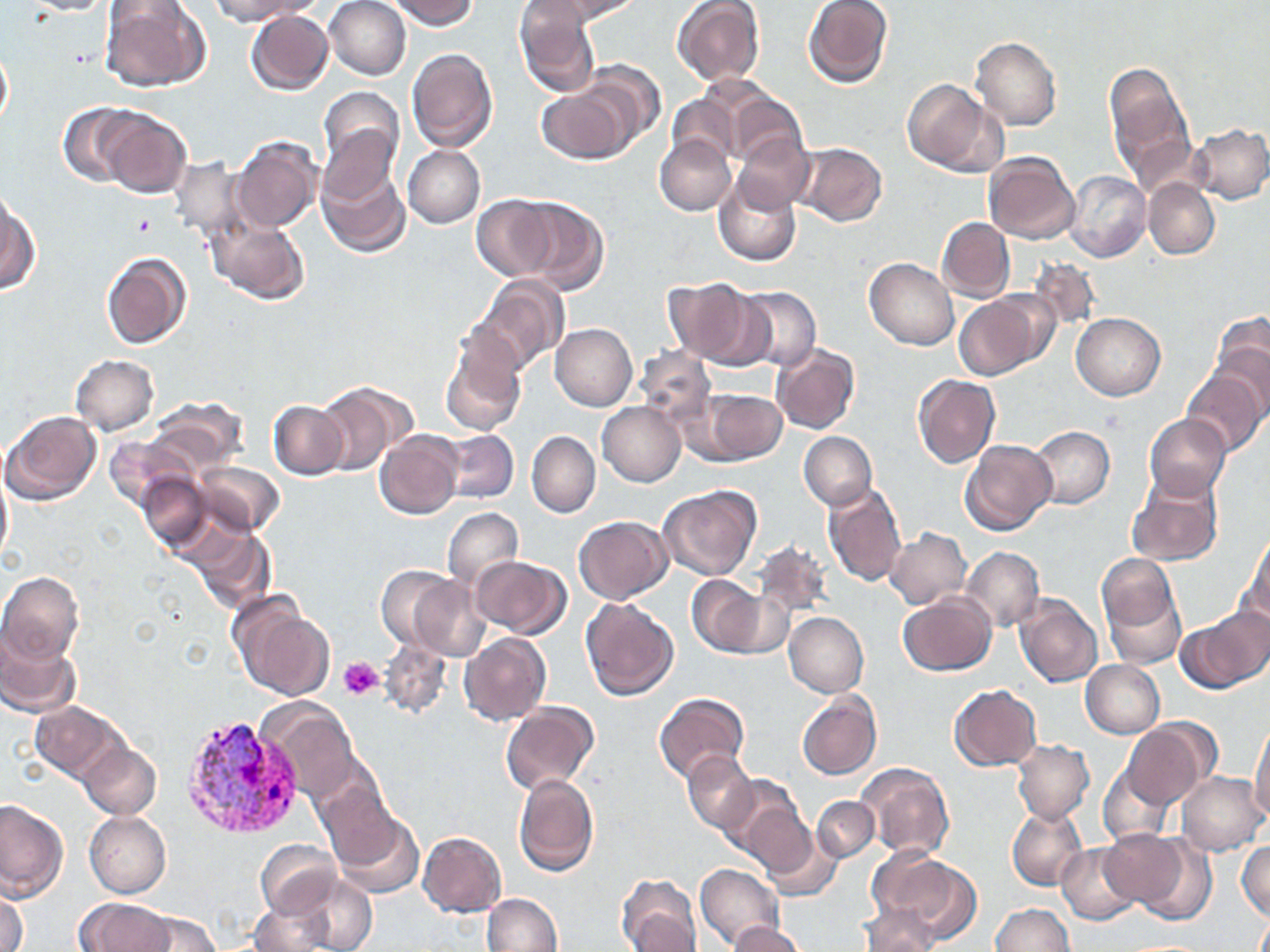

Summary:
  - Coordinate format: approximate bounding boxes as named x1/y1/x2/y2 corners in pixels
  - Platelet locations: (x1=129, y1=212, x2=158, y2=238), (x1=339, y1=656, x2=385, y2=699)
  - Plasmodium vivax-infected red blood cell locations: (x1=178, y1=711, x2=308, y2=837)
  - Uninfected red blood cell locations: (x1=20, y1=0, x2=122, y2=15), (x1=209, y1=0, x2=314, y2=25), (x1=325, y1=0, x2=412, y2=80), (x1=389, y1=0, x2=478, y2=30), (x1=551, y1=0, x2=642, y2=21), (x1=100, y1=1, x2=208, y2=92), (x1=672, y1=1, x2=766, y2=87), (x1=803, y1=1, x2=893, y2=88), (x1=513, y1=2, x2=600, y2=97), (x1=246, y1=11, x2=334, y2=96), (x1=972, y1=37, x2=1061, y2=130), (x1=0, y1=41, x2=12, y2=132), (x1=406, y1=48, x2=498, y2=152), (x1=574, y1=60, x2=665, y2=149), (x1=1104, y1=61, x2=1195, y2=186), (x1=900, y1=78, x2=1000, y2=174), (x1=536, y1=82, x2=638, y2=164), (x1=704, y1=82, x2=802, y2=166), (x1=318, y1=86, x2=404, y2=176), (x1=667, y1=91, x2=740, y2=166), (x1=57, y1=103, x2=140, y2=187), (x1=93, y1=107, x2=193, y2=198), (x1=1187, y1=123, x2=1270, y2=204), (x1=315, y1=124, x2=401, y2=214), (x1=230, y1=135, x2=322, y2=233), (x1=655, y1=135, x2=736, y2=216), (x1=732, y1=135, x2=814, y2=214), (x1=791, y1=144, x2=887, y2=227), (x1=403, y1=146, x2=485, y2=229), (x1=982, y1=151, x2=1080, y2=244), (x1=168, y1=155, x2=251, y2=240), (x1=317, y1=163, x2=410, y2=258), (x1=1066, y1=171, x2=1150, y2=263), (x1=713, y1=174, x2=803, y2=266), (x1=1144, y1=179, x2=1220, y2=259), (x1=515, y1=195, x2=609, y2=293), (x1=470, y1=196, x2=559, y2=280), (x1=1, y1=198, x2=38, y2=295), (x1=937, y1=217, x2=1015, y2=302), (x1=208, y1=219, x2=312, y2=305), (x1=101, y1=251, x2=191, y2=350), (x1=865, y1=258, x2=958, y2=350), (x1=1025, y1=258, x2=1101, y2=332), (x1=472, y1=276, x2=567, y2=375), (x1=662, y1=277, x2=759, y2=365), (x1=736, y1=287, x2=820, y2=372), (x1=956, y1=293, x2=1047, y2=380), (x1=1071, y1=312, x2=1165, y2=400), (x1=1209, y1=312, x2=1270, y2=415), (x1=551, y1=323, x2=637, y2=412), (x1=439, y1=340, x2=525, y2=437), (x1=772, y1=343, x2=860, y2=434), (x1=633, y1=347, x2=716, y2=425), (x1=71, y1=355, x2=158, y2=435), (x1=1182, y1=367, x2=1267, y2=456), (x1=913, y1=374, x2=999, y2=469), (x1=316, y1=382, x2=411, y2=474), (x1=692, y1=386, x2=788, y2=466), (x1=145, y1=398, x2=246, y2=475), (x1=268, y1=400, x2=348, y2=479), (x1=598, y1=401, x2=686, y2=486), (x1=2, y1=410, x2=102, y2=506), (x1=1144, y1=413, x2=1231, y2=501), (x1=1028, y1=426, x2=1115, y2=509), (x1=374, y1=430, x2=463, y2=519), (x1=440, y1=430, x2=518, y2=504), (x1=527, y1=431, x2=600, y2=518), (x1=798, y1=431, x2=877, y2=510), (x1=103, y1=436, x2=191, y2=511), (x1=961, y1=439, x2=1057, y2=536), (x1=190, y1=460, x2=286, y2=537), (x1=0, y1=464, x2=12, y2=569), (x1=137, y1=471, x2=214, y2=553), (x1=1127, y1=473, x2=1223, y2=567), (x1=823, y1=484, x2=906, y2=587), (x1=659, y1=485, x2=761, y2=580), (x1=442, y1=507, x2=522, y2=591), (x1=574, y1=516, x2=672, y2=604), (x1=183, y1=524, x2=276, y2=612), (x1=884, y1=528, x2=971, y2=608), (x1=1246, y1=533, x2=1270, y2=624), (x1=753, y1=539, x2=833, y2=622), (x1=961, y1=547, x2=1043, y2=632), (x1=1097, y1=554, x2=1180, y2=638), (x1=470, y1=555, x2=570, y2=638), (x1=376, y1=566, x2=461, y2=655), (x1=0, y1=571, x2=84, y2=665), (x1=407, y1=575, x2=491, y2=661), (x1=687, y1=575, x2=766, y2=656), (x1=720, y1=590, x2=795, y2=659), (x1=898, y1=591, x2=997, y2=675), (x1=1014, y1=593, x2=1102, y2=687), (x1=580, y1=596, x2=678, y2=700), (x1=232, y1=603, x2=335, y2=701), (x1=1183, y1=609, x2=1269, y2=691), (x1=785, y1=612, x2=868, y2=697), (x1=0, y1=627, x2=80, y2=717), (x1=459, y1=633, x2=551, y2=726), (x1=379, y1=641, x2=451, y2=720), (x1=1081, y1=660, x2=1164, y2=738), (x1=948, y1=684, x2=1041, y2=770), (x1=655, y1=692, x2=749, y2=784), (x1=796, y1=692, x2=880, y2=780), (x1=256, y1=696, x2=361, y2=800), (x1=31, y1=701, x2=127, y2=782), (x1=500, y1=702, x2=598, y2=796), (x1=1122, y1=721, x2=1212, y2=809), (x1=1250, y1=723, x2=1270, y2=822), (x1=1012, y1=740, x2=1094, y2=824), (x1=80, y1=744, x2=161, y2=818), (x1=683, y1=751, x2=757, y2=833), (x1=856, y1=762, x2=953, y2=860), (x1=1098, y1=765, x2=1174, y2=844), (x1=1177, y1=771, x2=1268, y2=854), (x1=513, y1=772, x2=598, y2=877), (x1=720, y1=776, x2=809, y2=870), (x1=317, y1=782, x2=407, y2=871), (x1=812, y1=796, x2=879, y2=861), (x1=0, y1=799, x2=66, y2=900), (x1=1007, y1=807, x2=1087, y2=891), (x1=328, y1=809, x2=426, y2=899), (x1=84, y1=811, x2=171, y2=898), (x1=746, y1=814, x2=834, y2=898), (x1=1099, y1=830, x2=1187, y2=909), (x1=1127, y1=830, x2=1218, y2=925), (x1=418, y1=832, x2=506, y2=917), (x1=256, y1=839, x2=340, y2=919), (x1=1238, y1=841, x2=1269, y2=921), (x1=1056, y1=843, x2=1143, y2=926), (x1=873, y1=851, x2=982, y2=944), (x1=695, y1=864, x2=783, y2=950), (x1=296, y1=874, x2=377, y2=952), (x1=616, y1=874, x2=700, y2=952), (x1=1, y1=888, x2=27, y2=952), (x1=481, y1=893, x2=561, y2=952), (x1=75, y1=898, x2=172, y2=951), (x1=248, y1=898, x2=332, y2=952), (x1=990, y1=903, x2=1074, y2=952), (x1=857, y1=904, x2=940, y2=951), (x1=134, y1=910, x2=218, y2=952), (x1=725, y1=920, x2=803, y2=952)
  - Slide-level diagnosis: Plasmodium vivax
  - Magnification: 1000x
  - Stain: May-Grünwald-Giemsa
  - Image size: 1270×952 pixels
  - Preparation: thin blood film
  - Field of view: one of a larger specimen
  - Modality: optical microscopy